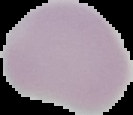

Summary:
  - Preparation: thin blood film
  - Malaria status: uninfected
  - Image size: 133×115 pixels
  - Image type: cell region segmented out of the field of view; surrounding area masked to black